State which parasite is depicted.
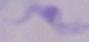
A trypanosome.

Summary:
  - Modality: photomicrograph
  - Magnification: 1000x